Name the parasite shown.
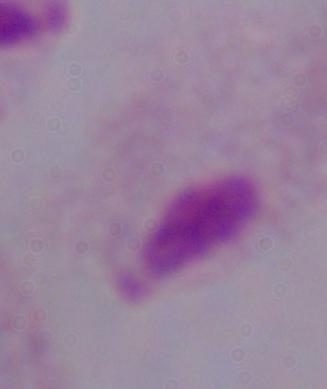
This is a trichomonad.

Summary:
  - Modality: micrograph
  - Magnification: 1000x